Describe the morphology of the red blood cells.
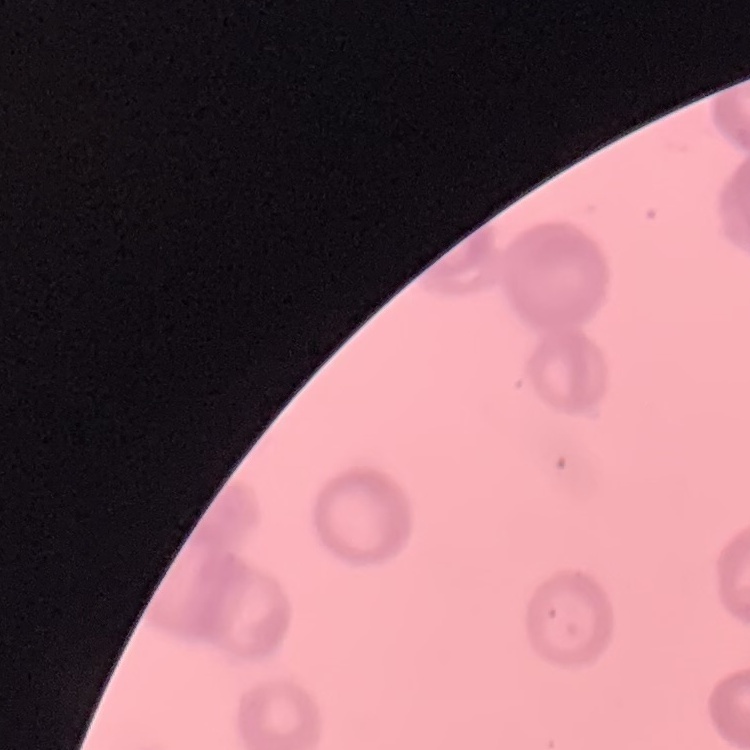
They show rouleaux formation.

image type = square crop of a larger photomicrograph
preparation = thin blood smear
stain = Field's or Giemsa